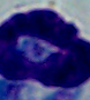

Captured at 1000x magnification. Photomicrograph. A leukocyte is shown.